Assess the morphology of the erythrocytes.
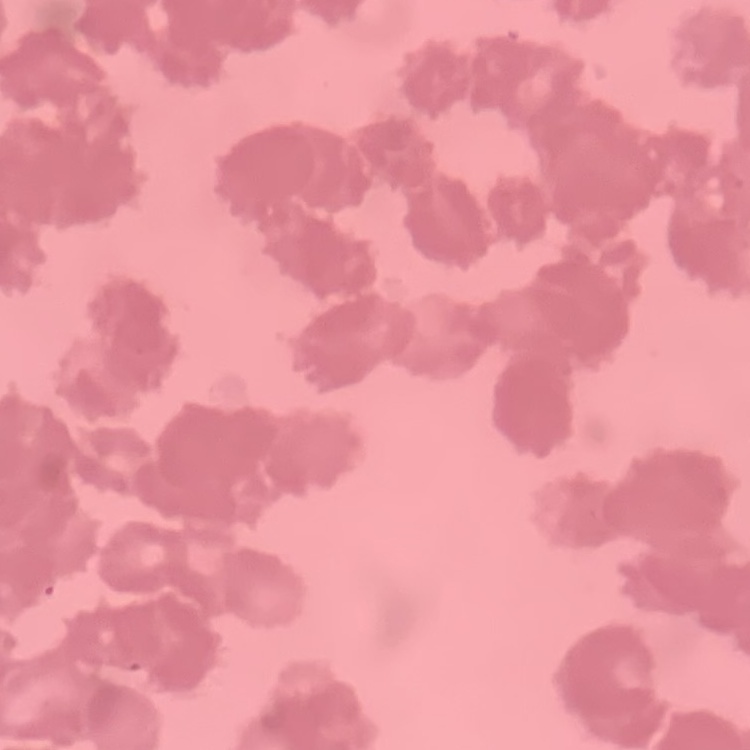

Rouleaux formation.

Field's or Giemsa stain. One tile cut from a larger photomicrograph. Thin peripheral smear.